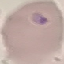
{
  "result": "no malaria parasites detected",
  "capture": "smartphone through the microscope eyepiece",
  "stain": "Giemsa",
  "preparation": "thin smear",
  "image_type": "automatically extracted cell patch, resized to 64 × 64 pixels"
}